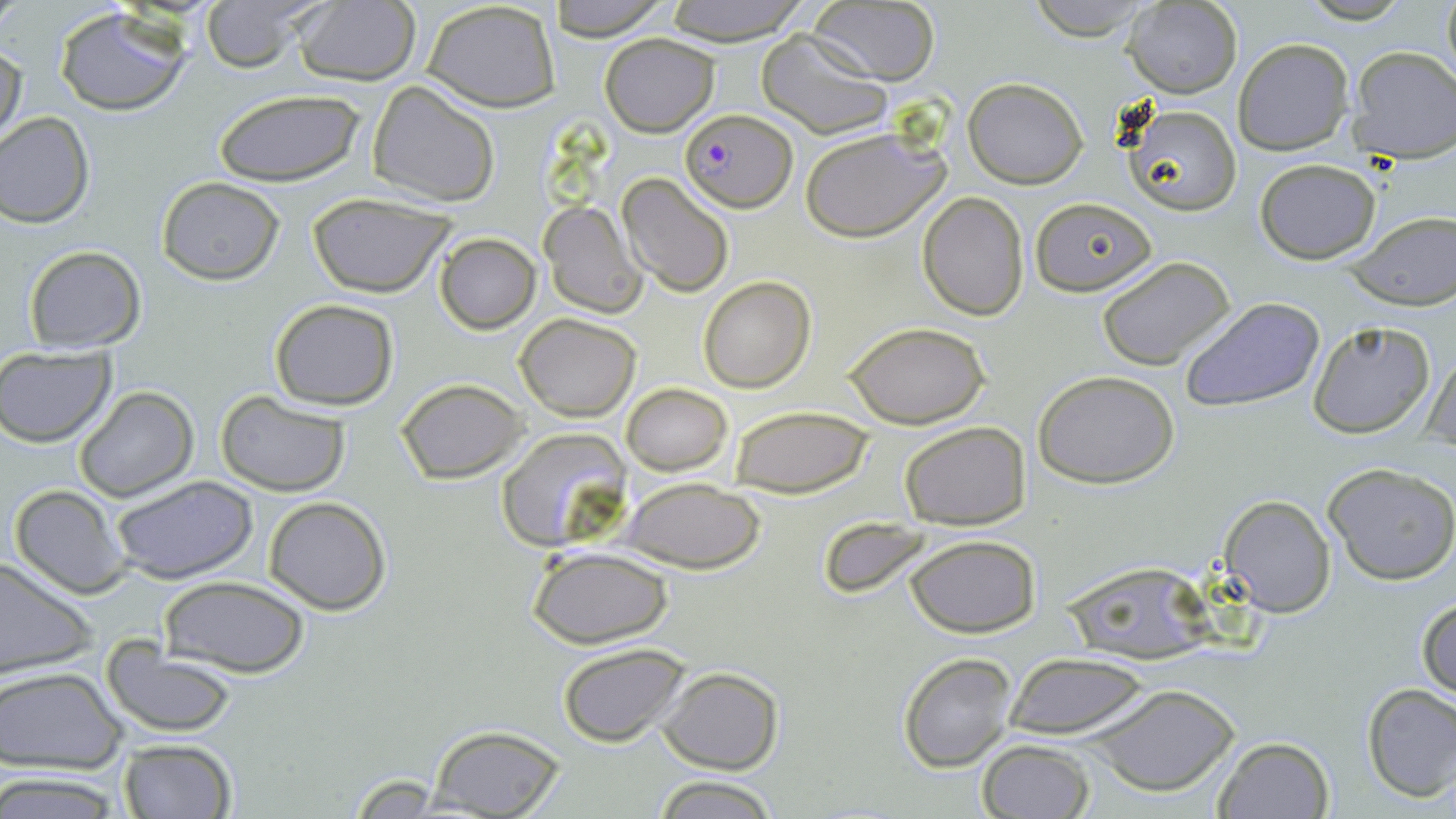

Summary:
  - Coordinate format: approximate bounding boxes as (x1, y1, x2, y2) in pixels
  - Plasmodium falciparum-infected red blood cell locations: (678, 109, 796, 213)
  - Uninfected red blood cell locations: (0, 0, 32, 32), (198, 0, 323, 74), (292, 0, 420, 85), (546, 0, 674, 41), (660, 0, 813, 45), (1022, 0, 1163, 41), (1441, 0, 1455, 82), (808, 1, 940, 85), (423, 2, 560, 111), (1123, 2, 1242, 97), (55, 8, 191, 116), (756, 30, 892, 138), (601, 33, 718, 137), (1234, 37, 1355, 156), (1, 42, 25, 149), (1347, 46, 1456, 162), (963, 77, 1088, 188), (367, 80, 500, 206), (212, 89, 365, 187), (1120, 102, 1243, 217), (0, 112, 94, 227), (800, 124, 952, 241), (1254, 159, 1381, 264), (617, 173, 736, 296), (156, 176, 285, 285), (917, 191, 1029, 320), (308, 194, 456, 298), (1029, 197, 1157, 295), (539, 201, 646, 318), (1343, 215, 1456, 308), (435, 233, 541, 334), (22, 245, 146, 352), (1096, 255, 1235, 370), (698, 275, 815, 392), (1181, 297, 1325, 414), (268, 298, 398, 409), (514, 314, 640, 420), (1307, 321, 1436, 439), (843, 322, 993, 428), (0, 347, 117, 447), (1423, 352, 1455, 455), (1033, 369, 1180, 488), (396, 379, 527, 483), (621, 383, 732, 476), (74, 385, 198, 501), (213, 390, 351, 494), (730, 404, 873, 496), (900, 422, 1029, 530), (494, 427, 633, 551), (1323, 462, 1456, 586), (110, 475, 260, 585), (622, 477, 765, 574), (9, 484, 132, 599), (1220, 494, 1336, 617), (264, 496, 391, 614), (826, 518, 930, 600), (905, 535, 1039, 637), (527, 547, 673, 647), (0, 557, 98, 680), (1063, 566, 1228, 667), (160, 576, 310, 676), (1416, 595, 1456, 701), (555, 643, 692, 747), (101, 646, 238, 737), (897, 651, 1017, 772), (1004, 654, 1150, 741), (0, 666, 127, 775), (657, 666, 784, 774), (1082, 681, 1241, 798), (1361, 683, 1456, 802), (424, 726, 567, 818), (1212, 735, 1336, 819), (117, 739, 237, 818), (976, 739, 1096, 819), (0, 771, 124, 816), (345, 774, 450, 813), (653, 775, 777, 819)
  - Slide-level diagnosis: Plasmodium falciparum
  - Field of view: one of a larger specimen
  - Modality: light microscopy
  - Magnification: 1000x
  - Stain: May-Grünwald-Giemsa
  - Image size: 1456×819 pixels
  - Preparation: thin blood film